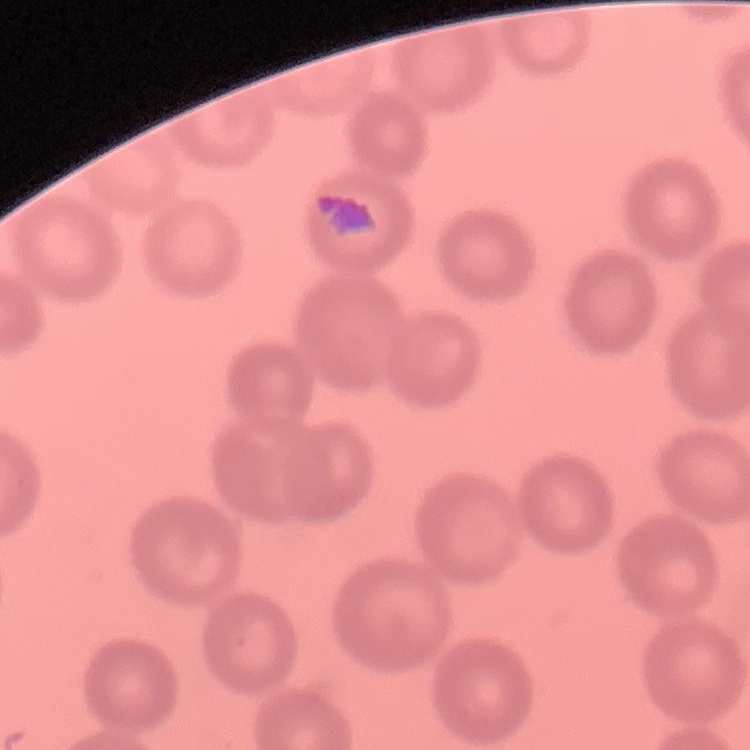
The red blood cells exhibit no rouleaux formation. Square crop of a larger photomicrograph. Thin blood film. Field's or Giemsa stain.